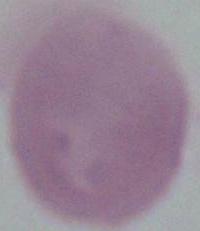

Summary:
  - Magnification: 1000x
  - Modality: photomicrograph
  - Identification: red blood cell